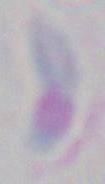

Micrograph. Captured at 1000x magnification. Toxoplasma gondii is shown.